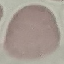

Result: no malaria parasites detected. Giemsa stain. Thin smear of blood. Acquired by smartphone through the microscope eyepiece. Cell patch, automatically extracted from a larger field of view and resized to 64 × 64 pixels.